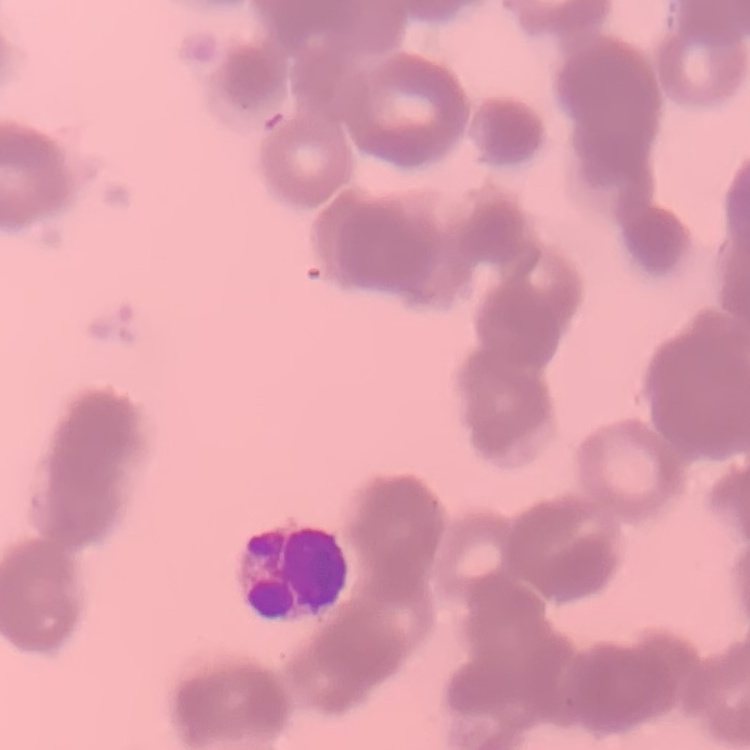
The erythrocytes exhibit rouleaux formation. One tile cut from a larger photomicrograph. Stained with either Field's or Giemsa. Thin peripheral smear.